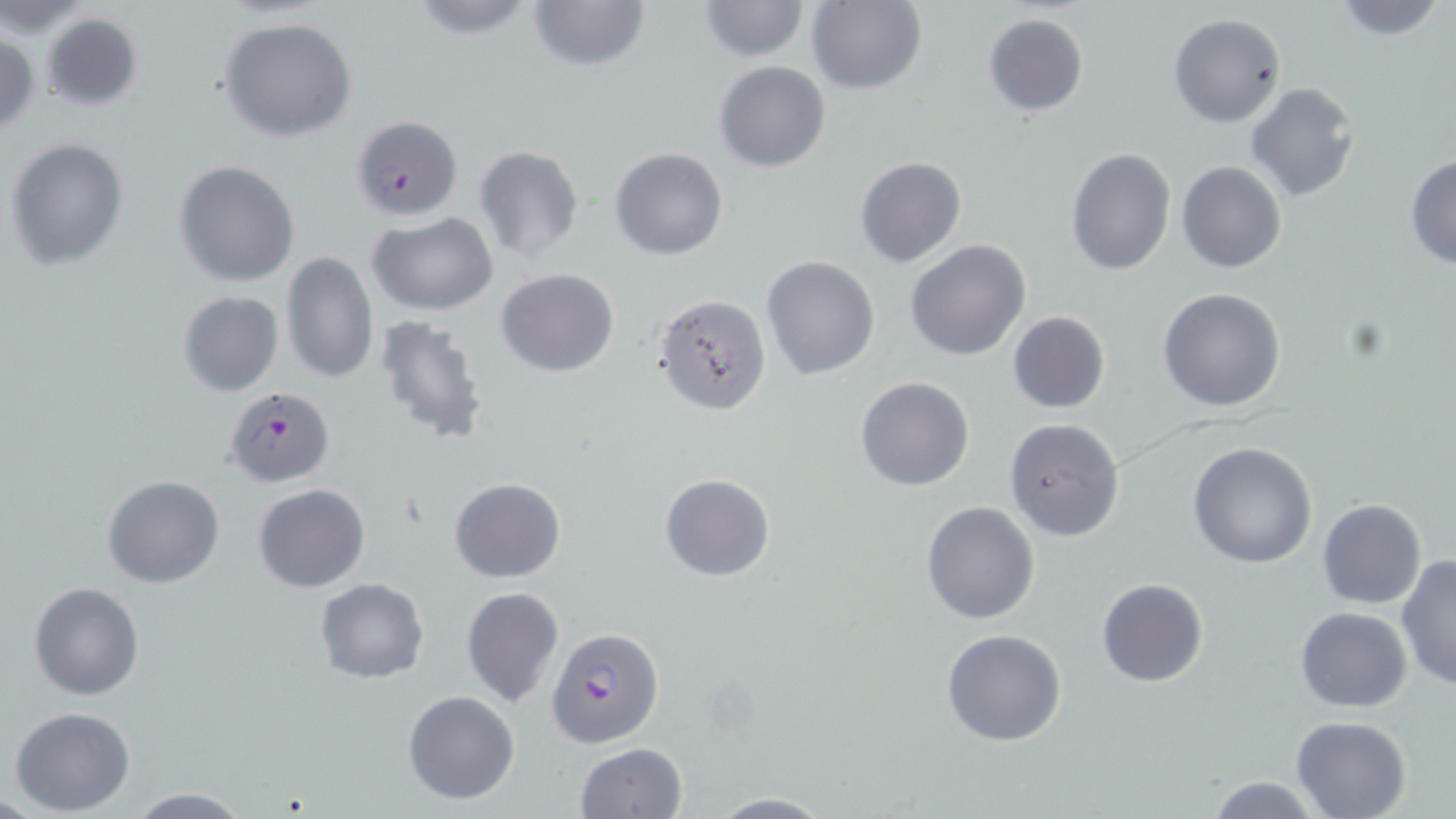
Summary:
  - Coordinate format: approximate bounding boxes as (x1,y1)-(x2,y2) corner pairs in pixels
  - Uninfected red blood cell locations: (402,0)-(545,43), (526,0)-(652,73), (696,0)-(810,61), (1328,0)-(1448,42), (807,1)-(927,95), (39,11)-(144,113), (983,12)-(1089,117), (1167,12)-(1286,128), (216,14)-(359,143), (0,30)-(40,138), (714,61)-(832,172), (1245,82)-(1360,203), (349,113)-(463,223), (5,136)-(130,270), (473,145)-(585,263), (610,147)-(727,260), (1066,148)-(1176,277), (1405,154)-(1456,269), (853,156)-(966,268), (173,160)-(302,287), (1177,160)-(1286,274), (366,213)-(498,314), (905,239)-(1032,361), (280,250)-(379,385), (761,255)-(880,381), (497,269)-(619,377), (1158,288)-(1286,413), (177,290)-(284,396), (653,294)-(772,416), (1007,311)-(1110,414), (371,314)-(491,447), (856,377)-(973,491), (1004,419)-(1125,541), (1187,441)-(1316,570), (658,472)-(775,581), (102,474)-(225,589), (448,478)-(566,584), (253,483)-(370,593), (1317,499)-(1426,609), (920,500)-(1040,624), (1396,556)-(1456,690), (1096,577)-(1207,688), (316,579)-(430,683), (29,581)-(144,700), (461,586)-(565,708), (1295,606)-(1413,712), (546,626)-(665,749), (942,629)-(1068,746), (403,691)-(520,805), (10,707)-(135,814), (1290,715)-(1413,819), (574,742)-(689,819), (1203,776)-(1324,817), (124,788)-(254,818), (704,792)-(836,817)
  - Plasmodium falciparum-infected red blood cell locations: (224,387)-(334,488)
  - Slide-level diagnosis: Plasmodium falciparum
  - Preparation: thin blood film
  - Field of view: one of a larger specimen
  - Image size: 1456×819 pixels
  - Modality: light microscopy
  - Magnification: 1000x
  - Stain: May-Grünwald-Giemsa